Identify the parasite.
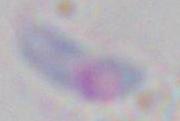
This is Toxoplasma gondii.

Captured at 1000x magnification. Micrograph.